Comment on the morphology of the red blood cells.
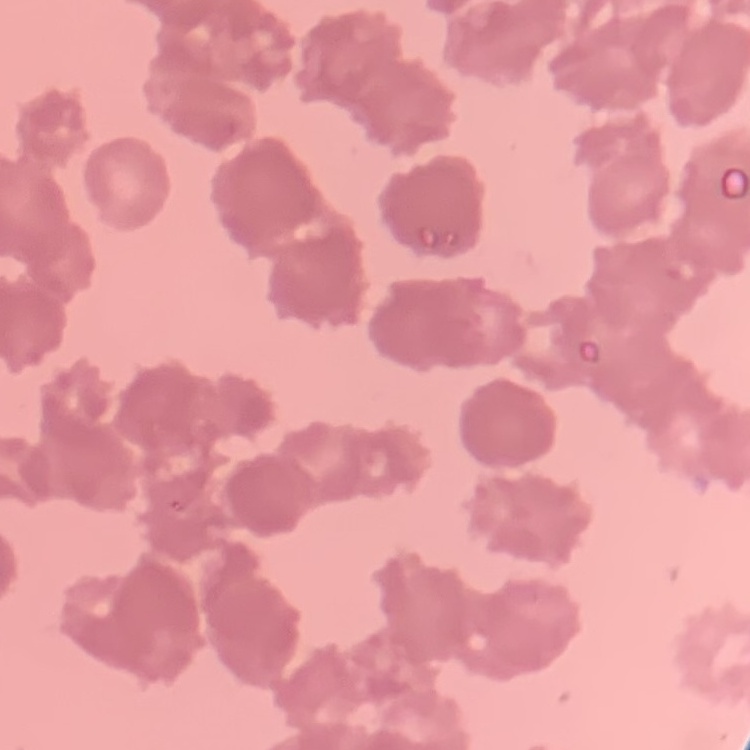
Rouleaux formation.

Summary:
  - Image type: one tile cut from a larger photomicrograph
  - Preparation: thin peripheral smear
  - Stain: Field's or Giemsa